Classify this cell by malaria status.
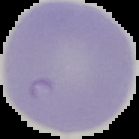

Uninfected.

Summary:
  - Image size: 139×139 pixels
  - Preparation: thin blood smear
  - Image type: segmented cell region on a black background